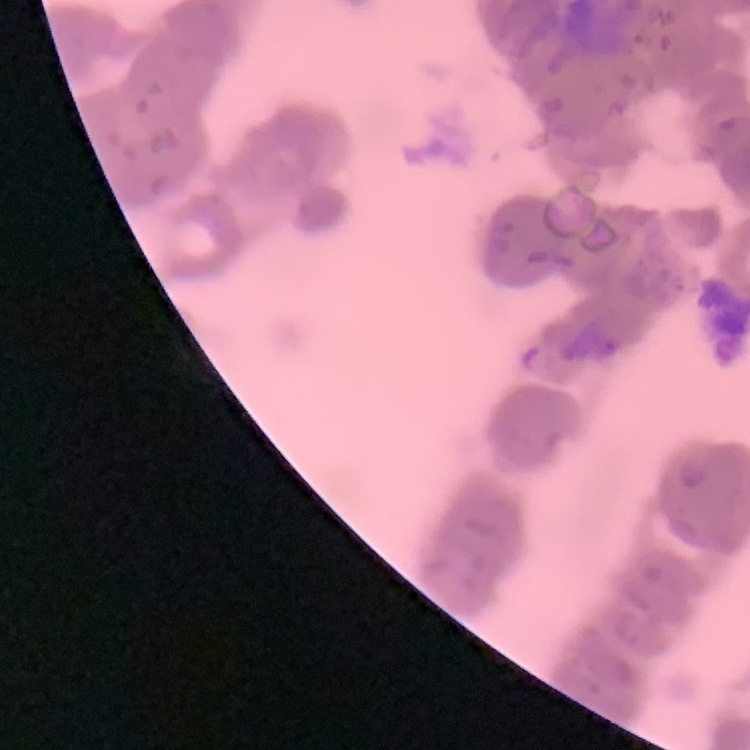

Summary:
  - Erythrocyte morphology: rouleaux formation
  - Preparation: thin blood film
  - Stain: Field's or Giemsa
  - Image type: one tile cut from a larger photomicrograph